Give the extent of all uninfected red blood cells.
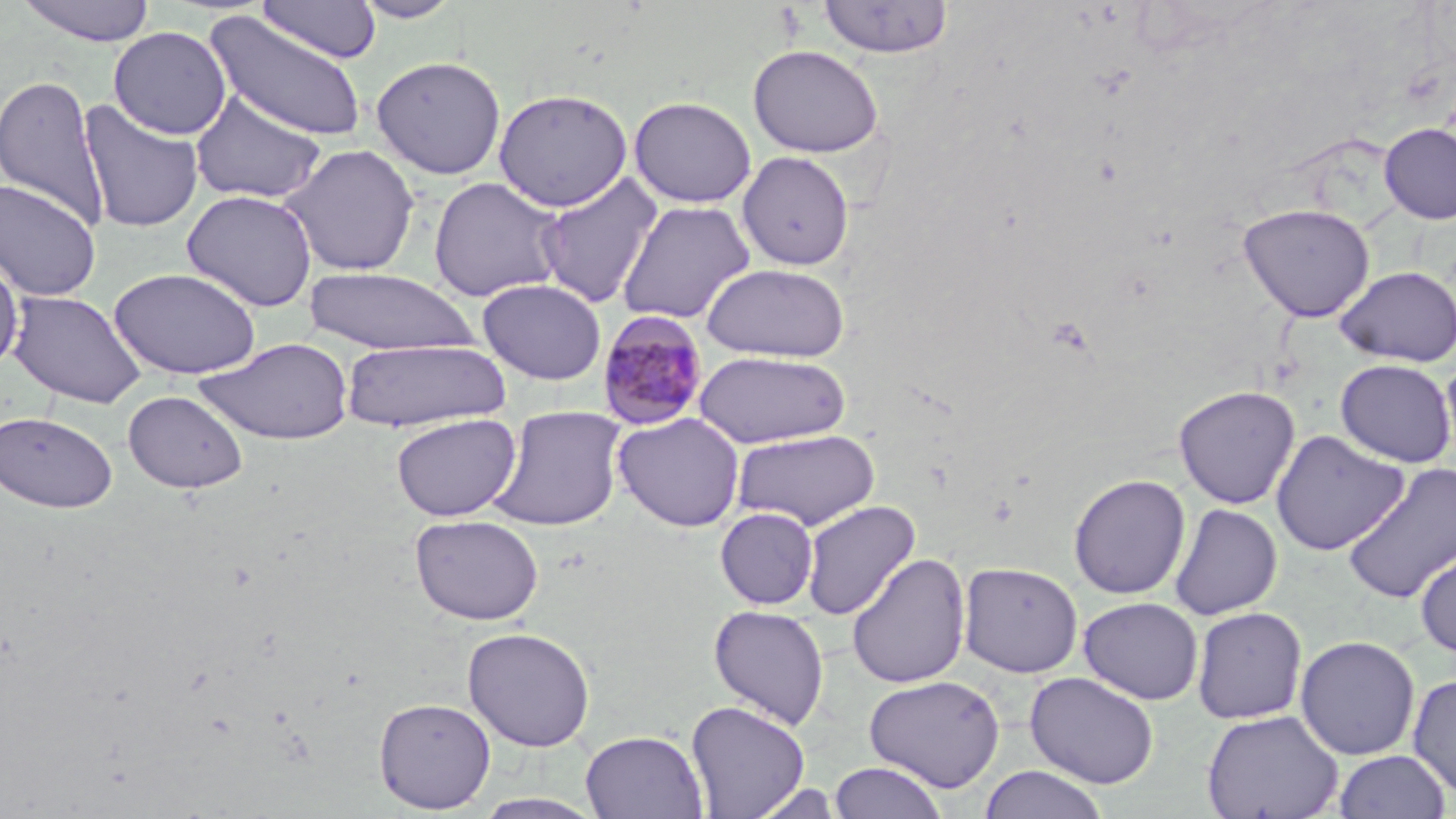
Approximate bounding boxes as (x1, y1, x2, y2) in pixels.
Uninfected red blood cells: (15, 0, 157, 46), (352, 0, 463, 23), (817, 0, 954, 60), (258, 1, 382, 63), (205, 11, 368, 143), (108, 26, 231, 139), (748, 44, 883, 158), (370, 55, 507, 179), (0, 74, 109, 229), (493, 88, 633, 212), (189, 90, 328, 204), (629, 95, 757, 208), (77, 99, 204, 234), (1379, 123, 1456, 224), (280, 143, 421, 277), (738, 151, 854, 270), (534, 172, 664, 308), (428, 176, 567, 302), (0, 178, 101, 301), (181, 189, 318, 312), (616, 200, 756, 324), (1238, 202, 1375, 322), (0, 253, 24, 374), (701, 263, 850, 362), (1334, 265, 1456, 367), (109, 267, 262, 379), (303, 267, 479, 355), (477, 278, 607, 385), (8, 289, 147, 408), (198, 337, 353, 445), (340, 339, 509, 431), (694, 350, 851, 449), (1440, 357, 1456, 468), (1335, 359, 1455, 467), (1173, 385, 1300, 509), (123, 390, 249, 493), (487, 404, 627, 531), (0, 411, 117, 514), (391, 413, 521, 521), (612, 413, 745, 532), (732, 428, 881, 531), (1270, 429, 1409, 556), (1342, 463, 1456, 604), (1068, 473, 1191, 600), (801, 500, 920, 620), (1169, 503, 1282, 619), (715, 507, 820, 609), (409, 513, 544, 625), (1415, 546, 1456, 658), (847, 552, 971, 689), (959, 561, 1083, 678), (1078, 596, 1203, 705), (708, 605, 830, 729), (1191, 607, 1308, 724), (462, 626, 596, 752), (1295, 635, 1420, 760), (1024, 671, 1159, 789), (1407, 672, 1456, 800), (863, 674, 1005, 793), (374, 697, 495, 813), (685, 699, 811, 818), (1201, 709, 1343, 819), (581, 729, 708, 818), (1333, 749, 1451, 819), (829, 761, 947, 819), (978, 765, 1110, 819), (472, 792, 607, 818).

Plasmodium malariae-infected red blood cell locations: (596, 310, 709, 431). Slide-level diagnosis: Plasmodium malariae. Image is 1456×819 pixels. Thin blood film. 1000x magnification. Single field of view. Light microscopy. May-Grünwald-Giemsa-stained preparation.